Report the malaria status of this cell.
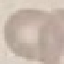
Uninfected.

Cell patch, automatically extracted from a larger field of view and resized to 64 × 64 pixels. Acquired by smartphone through the microscope eyepiece. Thin blood smear. Giemsa-stained preparation.